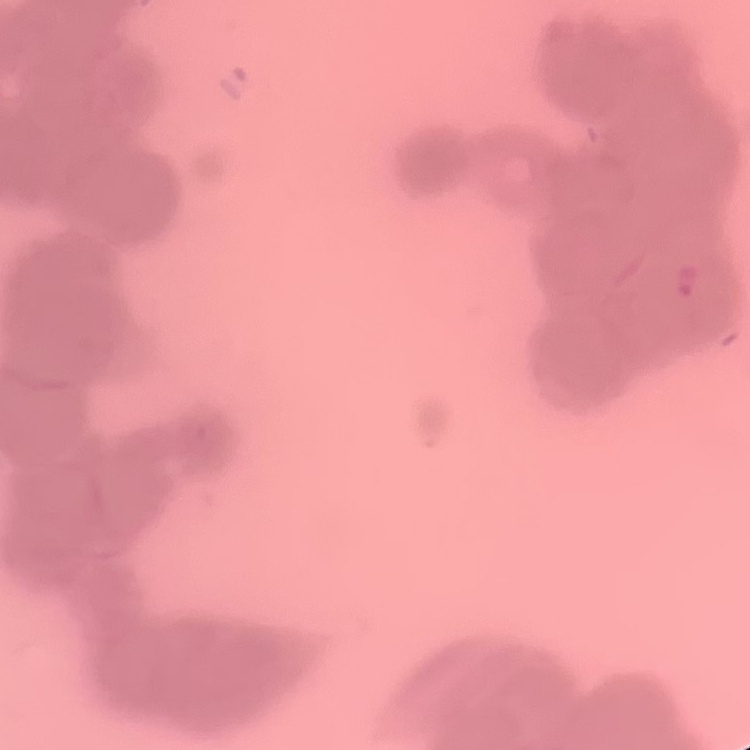
red blood cell morphology = rouleaux formation
preparation = thin blood smear
image type = square crop of a larger photomicrograph
stain = Field's or Giemsa